Give the position of every Plasmodium parasite visible.
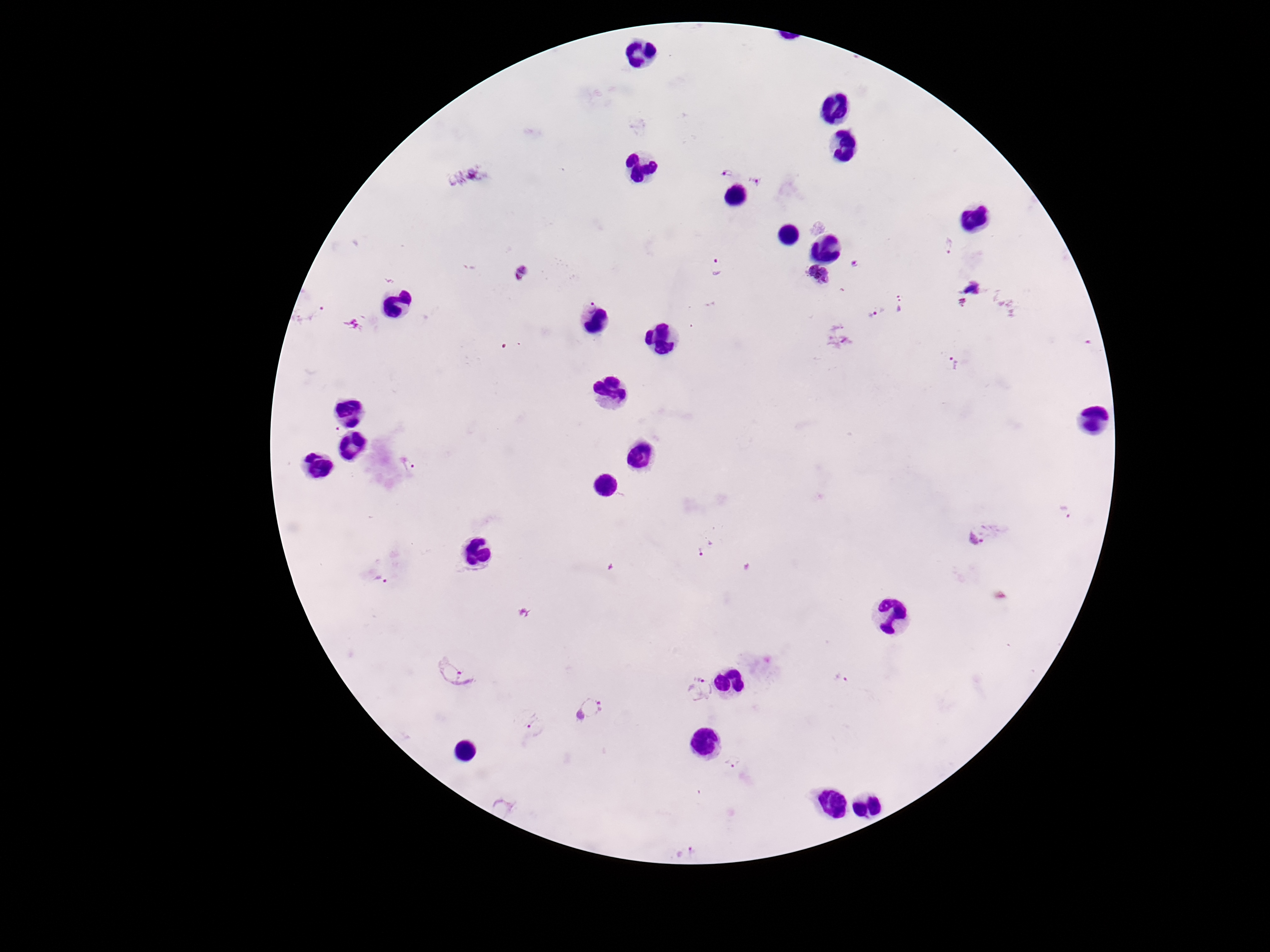

Approximate object centers, in pixels from the top-left corner.
Plasmodium parasites: (x=727, y=174), (x=467, y=176), (x=755, y=180), (x=949, y=246), (x=856, y=263), (x=717, y=269), (x=518, y=274), (x=818, y=277), (x=963, y=302), (x=589, y=304), (x=903, y=304), (x=877, y=313), (x=956, y=361), (x=341, y=431), (x=409, y=464), (x=1064, y=512), (x=982, y=533), (x=705, y=546), (x=379, y=579), (x=457, y=671), (x=842, y=678), (x=702, y=689), (x=591, y=708), (x=537, y=727), (x=732, y=762), (x=685, y=852).

Giemsa-stained preparation. Photographed through the microscope eyepiece with a smartphone camera. Patient malaria status: infected. 100x magnification. Thick blood film. Image is 1270×952 pixels. One field from this slide.